State which parasite is depicted.
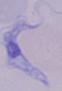
This is a trypanosome.

Summary:
  - Magnification: 1000x
  - Modality: micrograph